Point out each Plasmodium parasite.
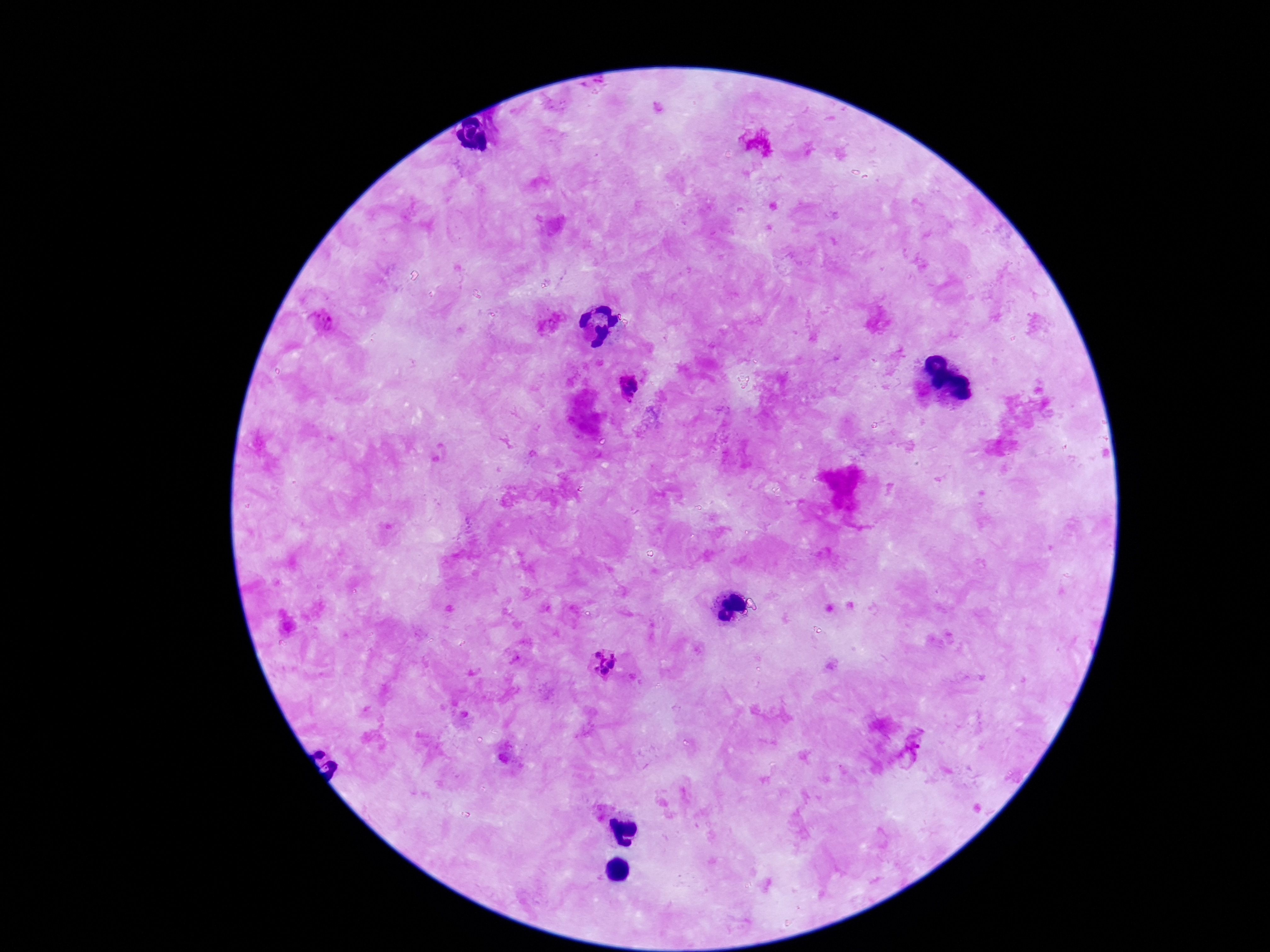

Approximate centers as [x, y] in pixels.
Plasmodium parasites: [321, 321], [628, 387], [598, 655], [612, 655], [600, 664], [611, 665], [604, 672], [913, 747].

Summary:
  - Patient malaria status: positive
  - Field of view: one from this slide
  - Image size: 1270×952 pixels
  - Stain: Giemsa
  - Magnification: 100x
  - Capture: smartphone camera through the microscope eyepiece
  - Preparation: thick blood film